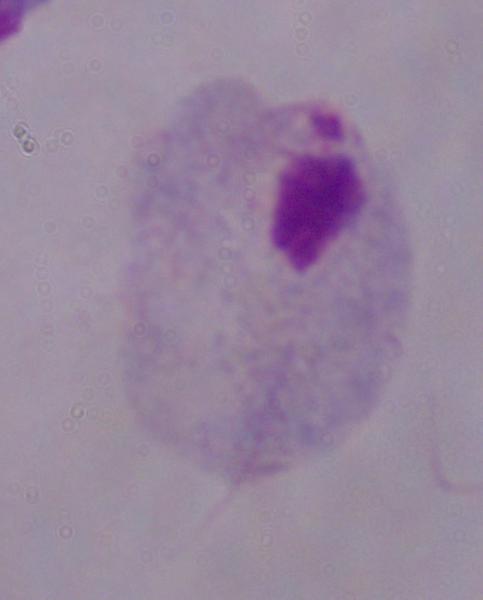
A trichomonad is seen. Micrograph. 1000x magnification.